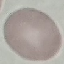
Result: negative for malaria parasites. Cell patch, automatically extracted from a larger field of view and resized to 64 × 64 pixels. Giemsa stain. Photographed with a smartphone camera at the microscope eyepiece. Thin smear of blood.